Point out each Plasmodium parasite.
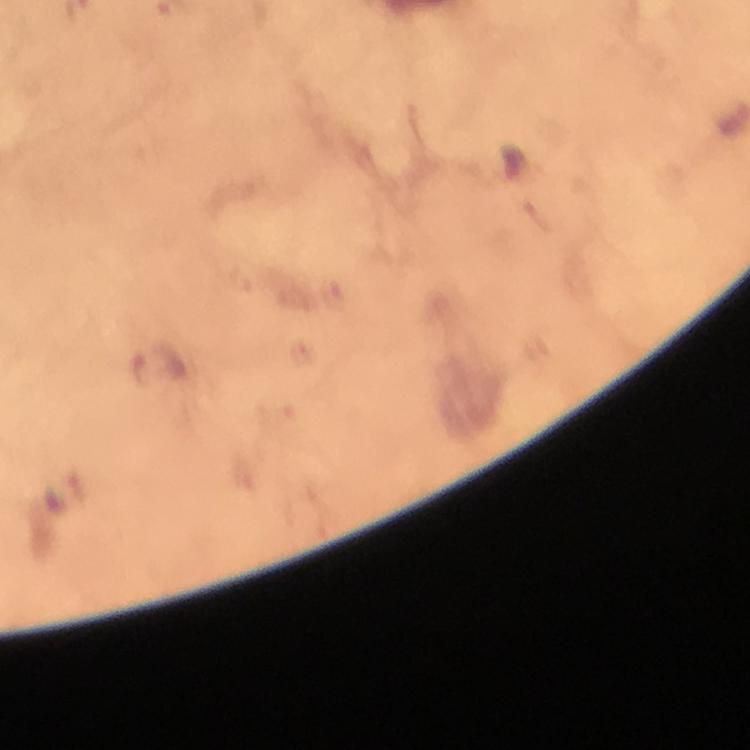

Approximate object centers, in pixels from the top-left corner.
Plasmodium parasites: (x=140, y=369), (x=77, y=487).

From a diagnostic examination for malaria. Immersion oil was used. Thick smear. Smartphone photograph taken through a microscope. Image is 750×750 pixels. At 100x magnification. Cropped region of a single field of view. Giemsa-stained preparation.